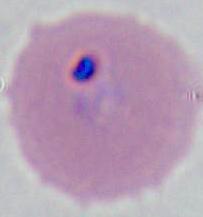
{
  "modality": "photomicrograph",
  "magnification": "400x or 1000x",
  "identification": "Plasmodium"
}